Describe the morphology of the erythrocytes.
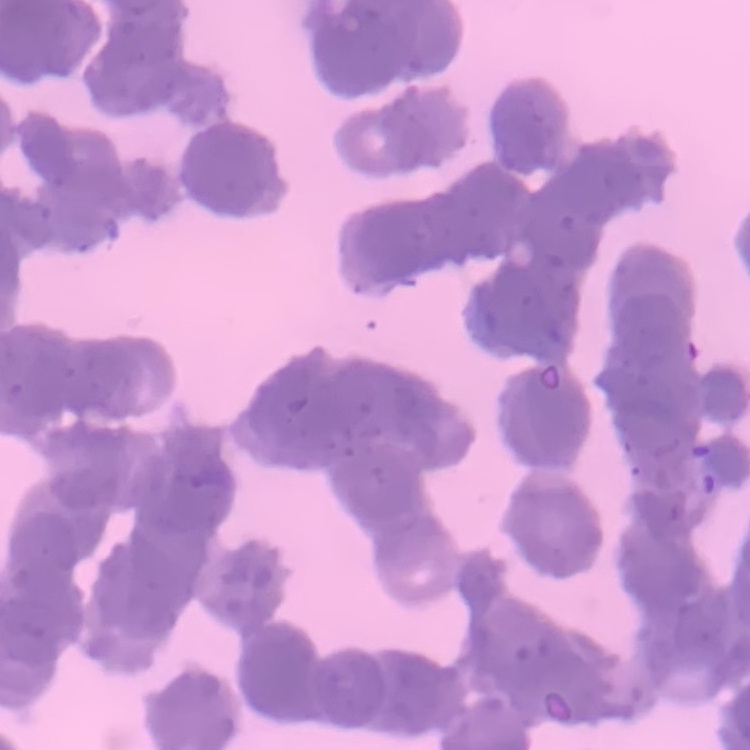
They show rouleaux formation.

image type = square crop of a larger photomicrograph
stain = Field's or Giemsa
preparation = thin blood film